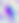

Summary:
  - Identification: Toxoplasma gondii
  - Modality: micrograph
  - Magnification: 400x